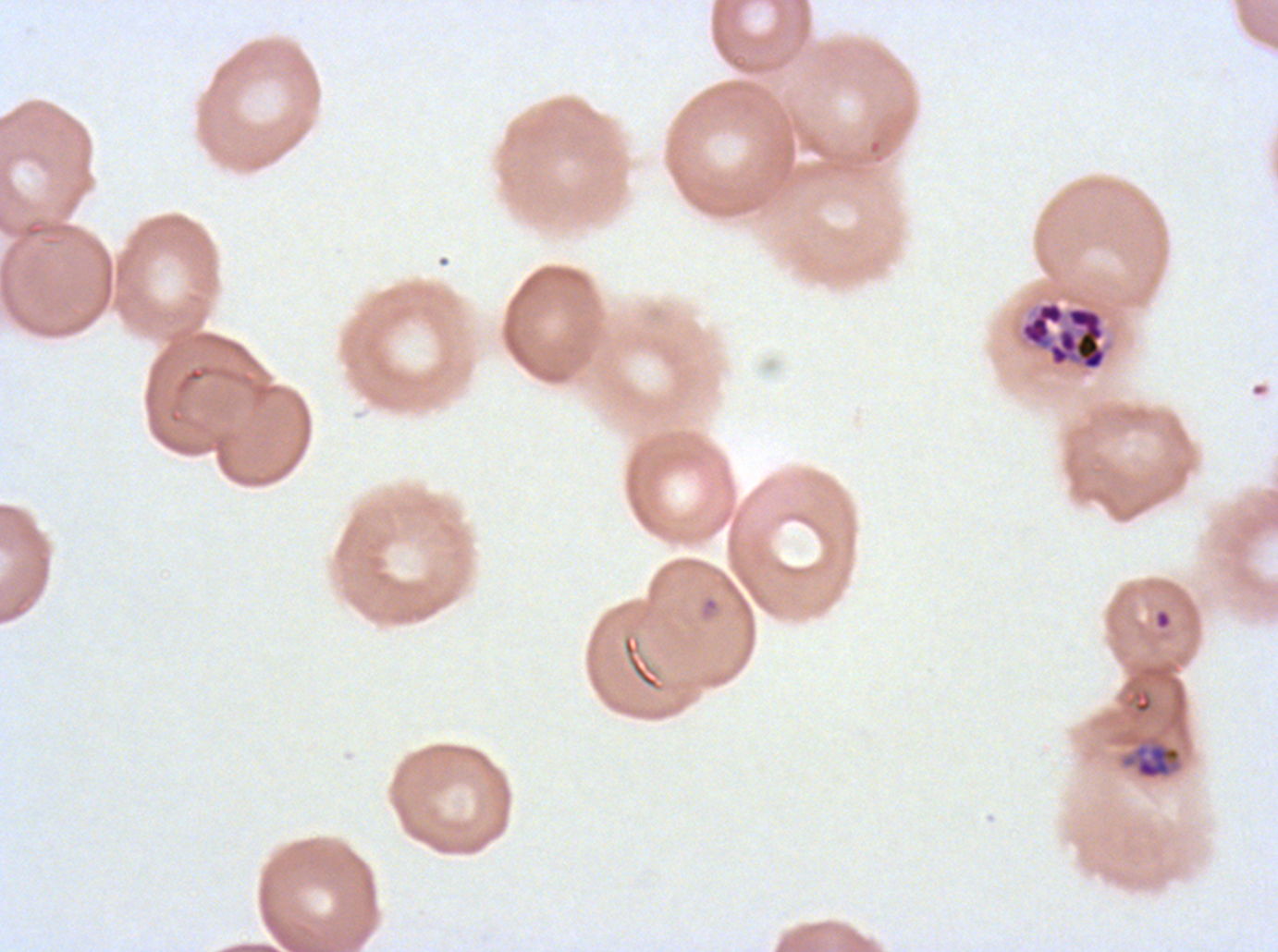

Approximate bounding rectangles given as corner coordinates in pixels from the top-left. Ring locations: (x1=1154, y1=609, x2=1172, y2=630), (x1=621, y1=634, x2=663, y2=692). Late schizont locations: (x1=1019, y1=300, x2=1108, y2=372), (x1=1123, y1=742, x2=1182, y2=780). Giemsa stain. P. falciparum from a patient in The Gambia, cultured ex vivo for 24 to 48 hours. Image is 1278×952 pixels. Thin blood film. A sub-image separated from a larger composite. Life-cycle stages observed: ring, late schizont.